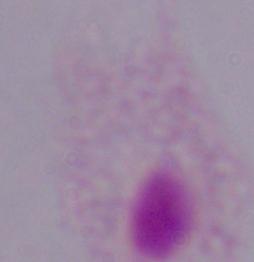
Summary:
  - Modality: photomicrograph
  - Magnification: 1000x
  - Identification: trichomonad